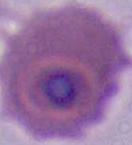 400x or 1000x magnification. A Plasmodium parasite is seen. Micrograph.